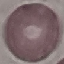
result = no malaria parasites detected
capture = smartphone camera at the microscope eyepiece
image type = cell patch, automatically extracted from a larger field of view and resized to 64 × 64 pixels
preparation = thin smear
stain = Giemsa